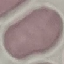

malaria_status: uninfected
image_type: cell patch, automatically extracted from a larger field of view and resized to 64 × 64 pixels
capture: smartphone camera at the microscope eyepiece
stain: Giemsa
preparation: thin smear